Assess this cell for malaria.
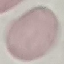

It is uninfected.

Summary:
  - Stain: Giemsa
  - Preparation: thin smear
  - Image type: automatically extracted cell patch, resized to 64 × 64 pixels
  - Capture: smartphone through the microscope eyepiece